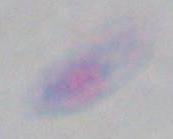
Summary:
  - Identification: Toxoplasma gondii
  - Magnification: 1000x
  - Modality: photomicrograph